Point out each leukocyte.
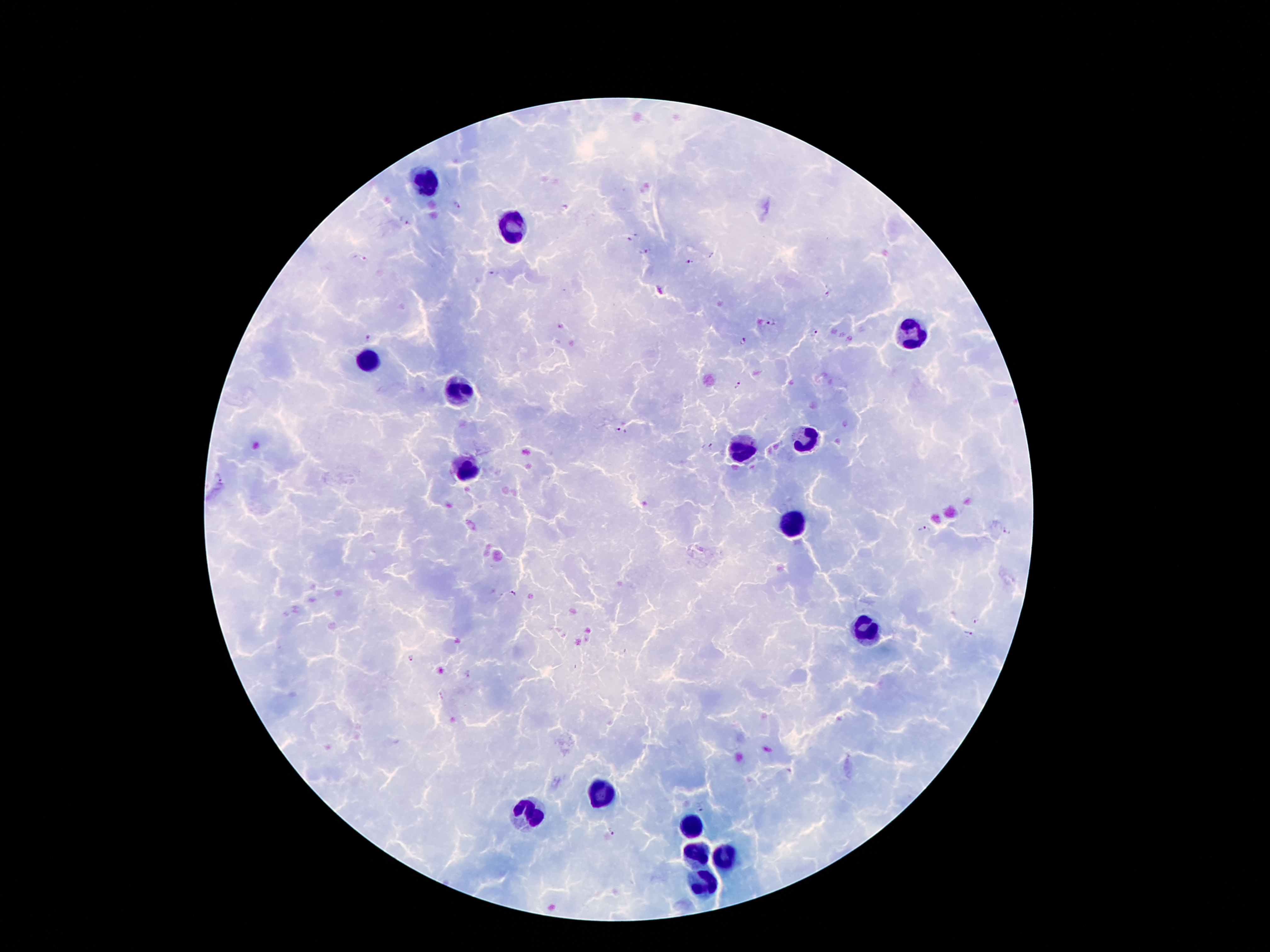
Approximate centers as {x, y} in pixels.
Leukocytes: {428, 184}, {509, 227}, {910, 333}, {366, 362}, {458, 389}, {805, 439}, {742, 451}, {465, 472}, {791, 524}, {868, 629}, {601, 794}, {528, 813}, {692, 824}, {696, 853}, {725, 857}, {703, 885}.

Malaria parasite locations: {455, 206}, {404, 220}, {633, 236}, {642, 251}, {713, 255}, {358, 258}, {689, 262}, {495, 272}, {827, 294}, {772, 321}, {813, 331}, {369, 339}, {743, 341}, {739, 386}, {620, 429}, {713, 447}, {218, 478}, {924, 530}, {1007, 533}, {511, 594}, {977, 620}, {968, 632}, {411, 657}, {700, 807}, {612, 830}. Giemsa stain. Patient malaria status: positive for Plasmodium falciparum. Single field of view. Image is 1270×952 pixels. Thick blood film. 100x magnification. Smartphone photograph taken through the microscope eyepiece.